Describe the morphology of the red blood cells.
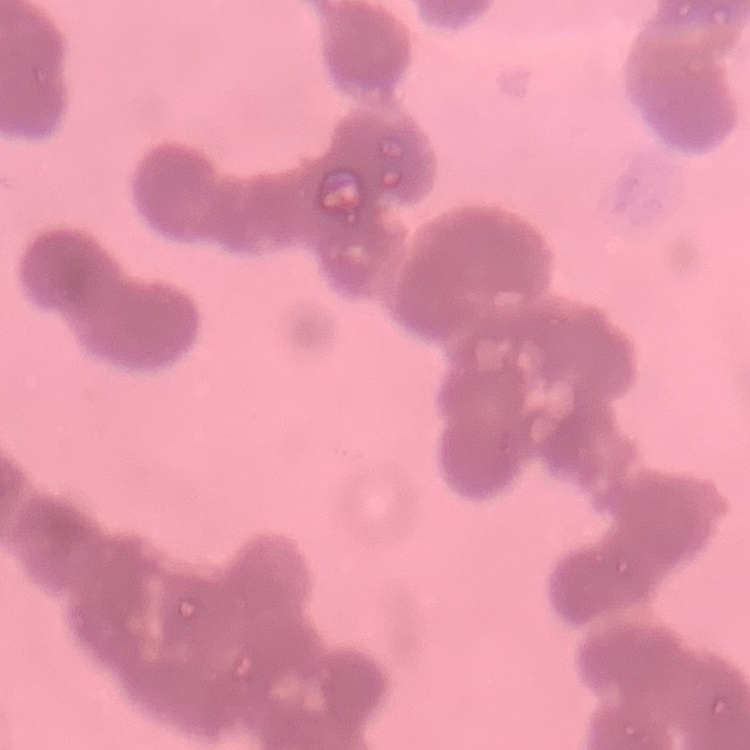

They show rouleaux formation.

image type = one tile cut from a larger photomicrograph
preparation = thin peripheral smear
stain = Field's or Giemsa